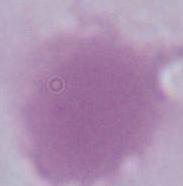
Summary:
  - Modality: photomicrograph
  - Magnification: 1000x
  - Identification: red blood cell